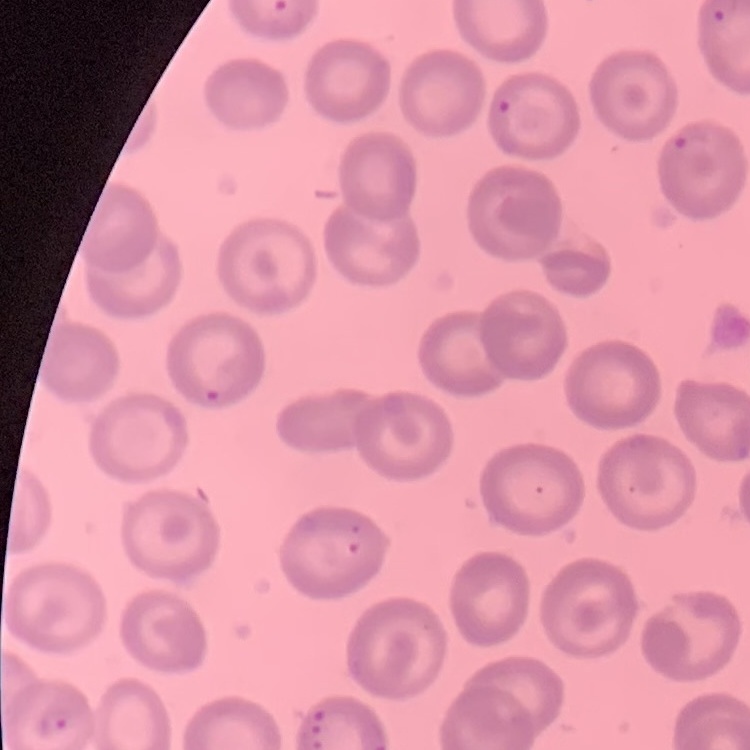

Summary:
  - Red blood cell morphology: no rouleaux formation
  - Image type: square crop of a larger photomicrograph
  - Preparation: thin blood film
  - Stain: Field's or Giemsa